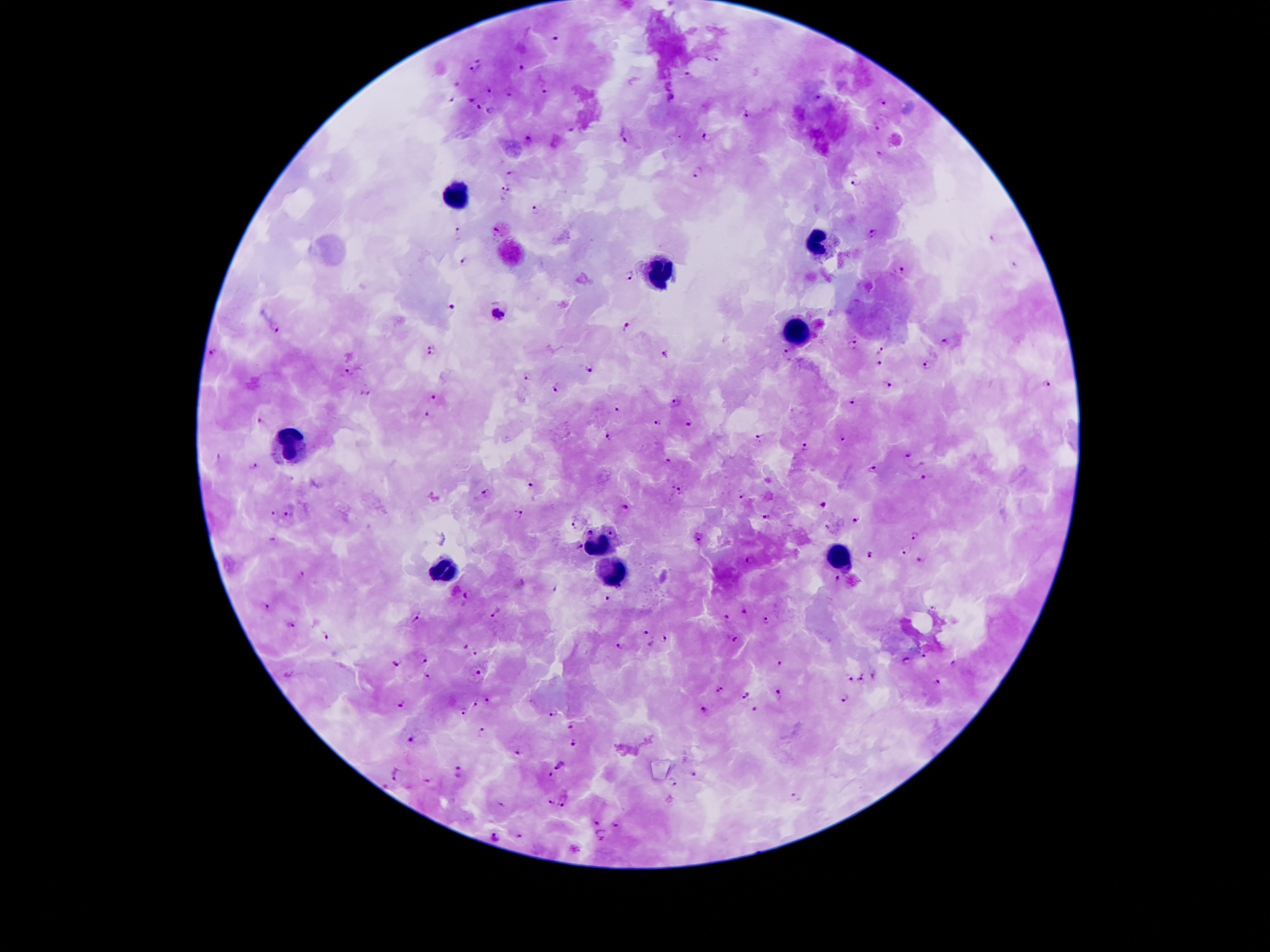 Approximate centers as [x, y] in pixels. Malaria parasite locations: [558, 35], [479, 56], [716, 60], [523, 67], [475, 72], [688, 75], [455, 84], [490, 89], [544, 90], [510, 93], [820, 95], [671, 96], [450, 99], [470, 99], [883, 104], [479, 106], [490, 111], [746, 113], [570, 127], [878, 128], [625, 137], [528, 138], [708, 138], [879, 154], [695, 173], [511, 174], [854, 184], [505, 188], [535, 210], [494, 229], [458, 233], [871, 233], [991, 236], [463, 259], [1014, 264], [900, 271], [630, 276], [451, 306], [500, 311], [627, 324], [274, 328], [944, 340], [854, 344], [881, 349], [432, 350], [213, 351], [785, 351], [663, 352], [880, 364], [928, 364], [590, 368], [353, 371], [526, 376], [1048, 384], [889, 385], [556, 388], [366, 392], [434, 395], [676, 399], [854, 401], [618, 410], [427, 414], [261, 422], [659, 422], [689, 423], [607, 434], [761, 437], [841, 438], [805, 446], [908, 454], [219, 459], [668, 460], [254, 466], [870, 468], [924, 476], [531, 485], [488, 492], [676, 492], [743, 494], [824, 504], [624, 509], [287, 514], [520, 514], [273, 515], [768, 517], [859, 519], [575, 526], [827, 527], [590, 531], [915, 534], [612, 535], [273, 539], [699, 539], [579, 548], [907, 551], [870, 557], [921, 559], [752, 560], [301, 573], [836, 576], [556, 588], [470, 594], [609, 599], [265, 607], [496, 612], [742, 612], [417, 617], [727, 619], [767, 621], [290, 624], [648, 632], [326, 634], [666, 638], [733, 640], [652, 643], [467, 645], [619, 646], [474, 653], [425, 656], [925, 658], [908, 660], [396, 662], [778, 662], [953, 664], [479, 672], [873, 674], [428, 675], [851, 679], [860, 680], [938, 681], [720, 690], [776, 693], [745, 695], [489, 698], [845, 698], [474, 703], [400, 704], [704, 710], [756, 710], [553, 711], [462, 713], [572, 726], [480, 730], [411, 738], [575, 741], [517, 752], [560, 765], [694, 772], [461, 773], [396, 774], [549, 776], [428, 780], [385, 783], [674, 783], [797, 798], [552, 801], [565, 801], [501, 804], [595, 822], [616, 824], [600, 834], [520, 835], [494, 836]. Leukocyte locations: [455, 194], [823, 243], [661, 274], [797, 334], [289, 440], [598, 545], [839, 562], [619, 567], [445, 572]. Patient malaria status: infected with Plasmodium falciparum. 100x magnification. Photographed through the microscope eyepiece with a smartphone camera. Giemsa stain. Thick peripheral-blood smear. One field from this slide. Image is 1270×952 pixels.